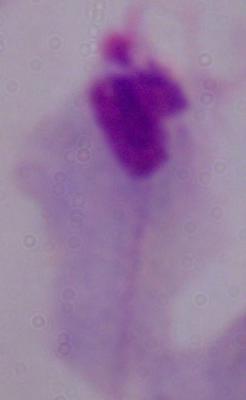
Summary:
  - Identification: trichomonad
  - Magnification: 1000x
  - Modality: photomicrograph